Outline each blood parasite and name the species.
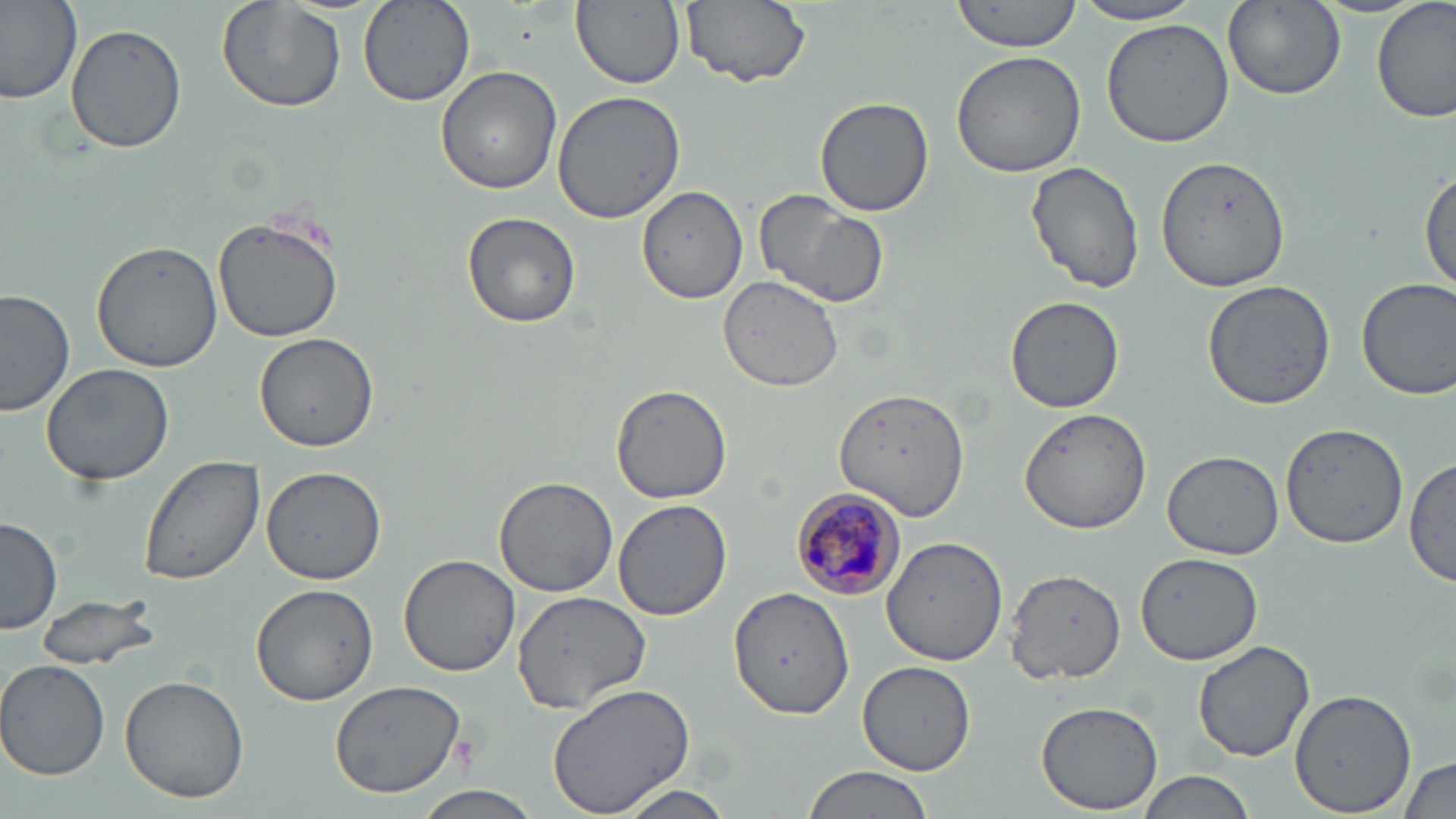
Approximate bounding boxes as (x1, y1, x2, y2) in pixels.
Plasmodium malariae-infected red blood cells: (793, 490, 907, 600).
No Plasmodium falciparum, Plasmodium ovale, Plasmodium vivax, Babesia divergens, or Trypanosoma brucei observed.

Summary:
  - Uninfected red blood cell locations: (356, 0, 473, 108), (572, 0, 685, 91), (680, 0, 812, 89), (950, 0, 1084, 54), (1222, 0, 1345, 101), (1374, 0, 1454, 122), (0, 1, 80, 107), (216, 1, 346, 114), (1073, 1, 1208, 26), (1101, 18, 1235, 147), (65, 21, 189, 154), (949, 50, 1086, 178), (436, 66, 562, 194), (551, 91, 685, 224), (814, 95, 934, 217), (1156, 153, 1293, 290), (1026, 160, 1145, 295), (1420, 173, 1455, 299), (638, 183, 748, 303), (754, 189, 892, 310), (461, 213, 581, 329), (212, 214, 346, 341), (89, 242, 222, 373), (719, 275, 845, 391), (1356, 277, 1456, 401), (1200, 279, 1339, 411), (0, 287, 75, 418), (1005, 293, 1126, 414), (254, 332, 380, 453), (39, 361, 174, 487), (610, 385, 732, 503), (834, 390, 969, 520), (1017, 406, 1156, 535), (1279, 422, 1408, 548), (1162, 450, 1284, 560), (139, 456, 266, 587), (1405, 456, 1456, 588), (259, 464, 386, 586), (493, 476, 620, 598), (611, 499, 735, 621), (1, 518, 63, 636), (880, 535, 1006, 666), (1134, 552, 1263, 665), (398, 555, 523, 677), (1005, 568, 1128, 681), (249, 582, 380, 705), (729, 585, 855, 719), (510, 590, 656, 716), (34, 593, 164, 673), (1193, 640, 1315, 763), (856, 660, 978, 776), (1, 661, 108, 780), (119, 673, 250, 805), (331, 680, 467, 797), (546, 682, 694, 817), (1289, 689, 1417, 816), (1035, 701, 1166, 815), (1397, 756, 1456, 819), (801, 764, 934, 819), (1138, 770, 1257, 819), (611, 783, 739, 819), (413, 785, 541, 819)
  - Slide-level diagnosis: Plasmodium malariae
  - Magnification: 1000x
  - Field of view: single
  - Modality: optical microscopy
  - Image size: 1456×819 pixels
  - Stain: May-Grünwald-Giemsa
  - Preparation: thin blood smear